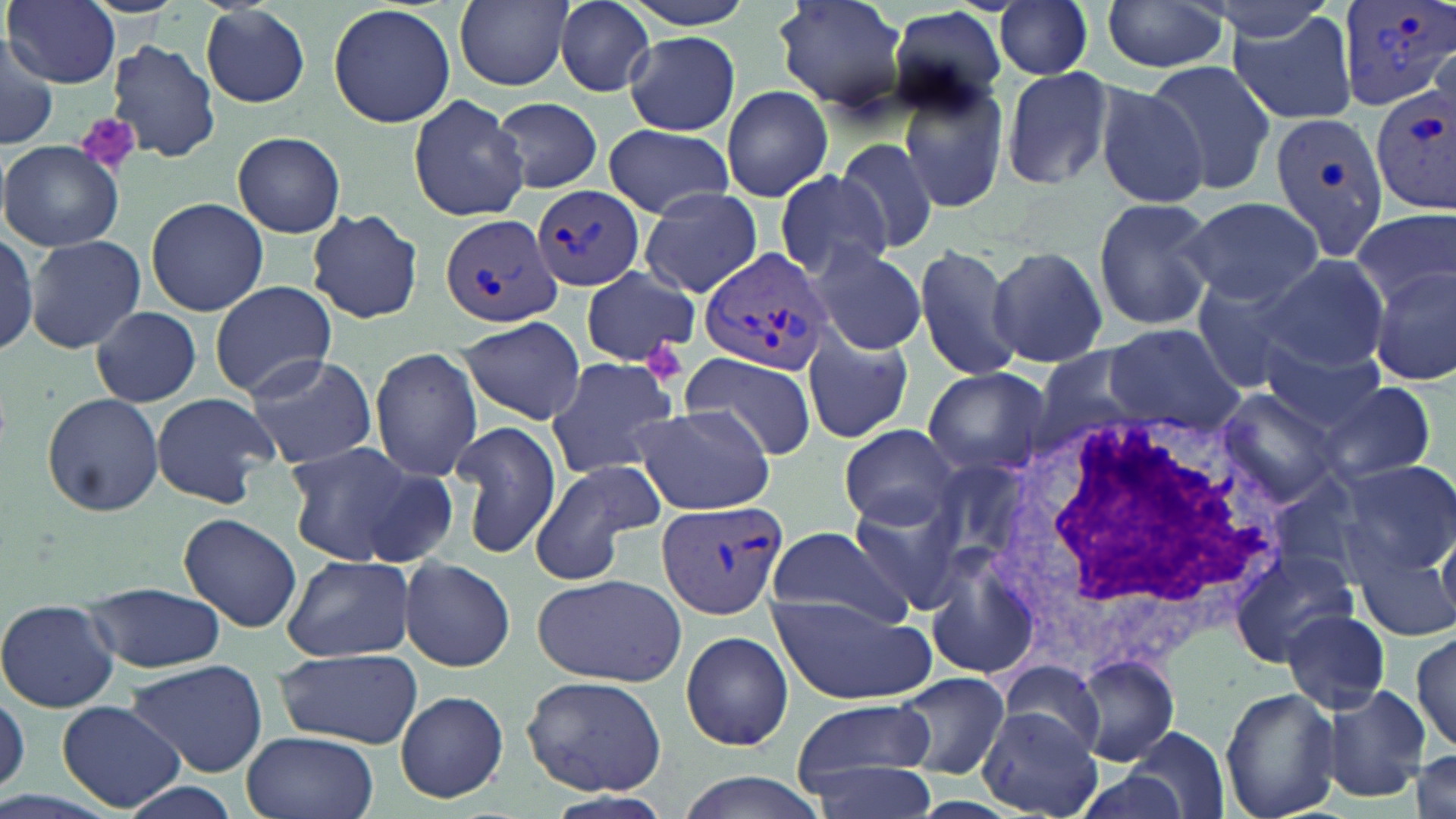
Summary:
  - Coordinate format: approximate bounding boxes as (x1,y1)-(x2,y2) corner pairs in pixels
  - Uninfected red blood cell locations: (7,0)-(120,87), (454,0)-(572,90), (620,0)-(754,31), (773,0)-(908,112), (995,0)-(1095,81), (1199,0)-(1341,45), (1100,1)-(1230,75), (554,2)-(656,97), (200,3)-(312,109), (328,3)-(454,129), (888,5)-(1011,113), (1224,7)-(1360,127), (624,32)-(739,135), (0,36)-(59,151), (106,39)-(219,164), (1143,60)-(1277,197), (1000,65)-(1118,193), (897,75)-(1010,214), (1094,81)-(1211,208), (721,85)-(834,202), (407,93)-(530,224), (489,95)-(602,195), (603,124)-(733,216), (232,132)-(346,238), (834,137)-(942,259), (2,141)-(124,251), (5,169)-(137,318), (772,169)-(889,283), (638,188)-(764,298), (145,196)-(269,316), (1092,196)-(1217,331), (1180,197)-(1323,307), (1188,202)-(1355,381), (305,208)-(425,324), (1352,208)-(1455,307), (0,228)-(37,358), (24,233)-(147,354), (911,241)-(1025,384), (809,242)-(927,357), (988,245)-(1107,368), (1258,253)-(1390,372), (1367,267)-(1456,386), (581,268)-(699,365), (1190,272)-(1317,392), (210,280)-(336,397), (92,306)-(201,408), (456,315)-(587,425), (1102,324)-(1246,433), (800,330)-(914,444), (1260,341)-(1389,436), (369,347)-(482,482), (682,350)-(815,461), (240,352)-(377,468), (544,354)-(681,482), (922,366)-(1052,478), (1315,382)-(1437,483), (1215,389)-(1345,507), (41,392)-(164,517), (150,393)-(281,509), (628,404)-(777,516), (448,419)-(560,561), (839,424)-(959,529), (281,440)-(433,568), (1326,457)-(1456,579), (527,458)-(666,587), (347,461)-(462,569), (847,492)-(965,609), (179,513)-(301,632), (766,525)-(912,631), (924,539)-(1046,683), (1232,547)-(1353,676), (1349,548)-(1455,645), (283,553)-(415,662), (401,557)-(516,671), (531,573)-(687,685), (83,581)-(226,674), (768,592)-(937,706), (0,597)-(120,713), (1282,610)-(1391,714), (1411,627)-(1455,754), (680,630)-(794,752), (274,648)-(422,748), (1067,655)-(1181,766), (126,658)-(268,778), (995,665)-(1108,760), (891,670)-(1009,779), (522,675)-(667,793), (1321,685)-(1430,803), (1220,686)-(1341,819), (0,687)-(28,798), (393,689)-(509,803), (57,700)-(186,814), (791,700)-(936,791), (977,704)-(1103,819), (1124,725)-(1228,817), (242,730)-(377,819), (1410,747)-(1455,819), (798,749)-(944,817), (662,772)-(834,819), (112,779)-(246,819), (545,789)-(676,818)
  - White blood cell locations: (984,410)-(1296,674)
  - Platelet locations: (76,113)-(141,174), (645,338)-(689,384)
  - Plasmodium vivax-infected red blood cell locations: (1336,0)-(1455,110), (1372,88)-(1456,210), (1265,108)-(1386,258), (534,183)-(646,293), (440,215)-(562,329), (697,246)-(834,374), (653,500)-(785,622)
  - Slide-level diagnosis: Plasmodium vivax
  - Stain: May-Grünwald-Giemsa
  - Image size: 1456×819 pixels
  - Field of view: single
  - Magnification: 1000x
  - Preparation: thin blood film
  - Modality: optical microscopy